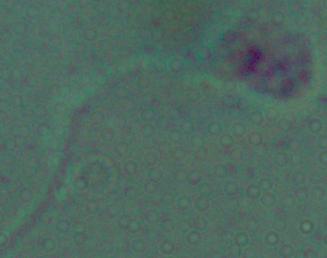

Summary:
  - Modality: micrograph
  - Identification: Leishmania
  - Magnification: 1000x